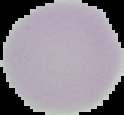

From a thin blood smear. Image is 124×115 pixels. Malaria status: uninfected. Segmented cell region on a black background.